Classify this cell by malaria status.
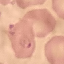
It is parasitized.

Summary:
  - Stain: Giemsa
  - Capture: smartphone through the microscope eyepiece
  - Image type: automatically extracted cell patch, resized to 64 × 64 pixels
  - Preparation: thin blood film